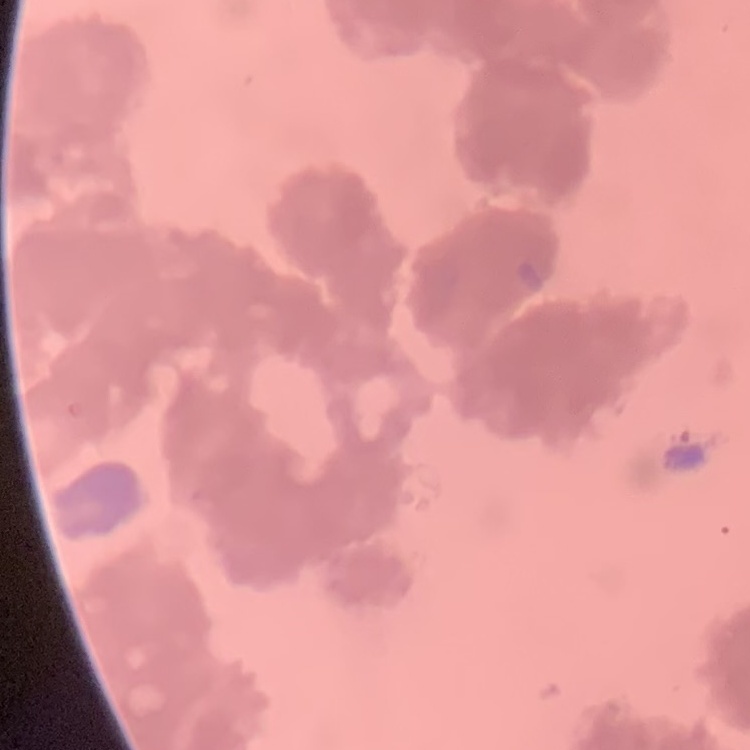

Summary:
  - Red blood cell morphology: rouleaux formation
  - Stain: Field's or Giemsa
  - Image type: one tile cut from a larger photomicrograph
  - Preparation: thin peripheral smear